Identify the parasite.
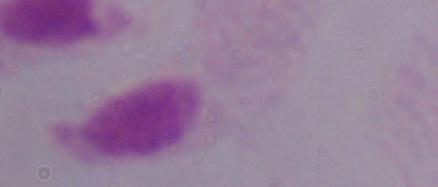

This is a trichomonad.

Summary:
  - Modality: micrograph
  - Magnification: 1000x